Classify this cell by malaria status.
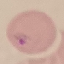
Parasitized.

Giemsa-stained preparation. Automatically extracted cell patch, resized to 64 × 64 pixels. Acquired by smartphone through the microscope eyepiece. Thin blood film.